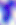
modality = micrograph
magnification = 400x
identification = Toxoplasma gondii